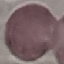

Summary:
  - Malaria status: uninfected
  - Image type: cell patch, automatically extracted from a larger field of view and resized to 64 × 64 pixels
  - Stain: Giemsa
  - Preparation: thin smear
  - Capture: smartphone through the microscope eyepiece